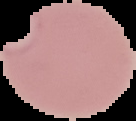
Summary:
  - Image type: segmented cell region with the area outside set to black
  - Preparation: thin blood film
  - Image size: 136×121 pixels
  - Result: malaria parasites detected